Report the malaria status of this cell.
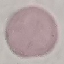
It is uninfected.

Thin smear of blood. Automatically extracted cell patch, resized to 64 × 64 pixels. Giemsa stain. Photographed with a smartphone camera at the microscope eyepiece.